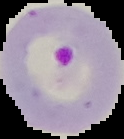

From a thin blood smear. Image is 124×139 pixels. Cell region segmented out of the field of view; the surrounding area is masked to black. Result: Plasmodium parasites identified.